Name the cell type shown.
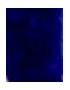

This is a leukocyte.

{
  "modality": "photomicrograph",
  "magnification": "1000x"
}